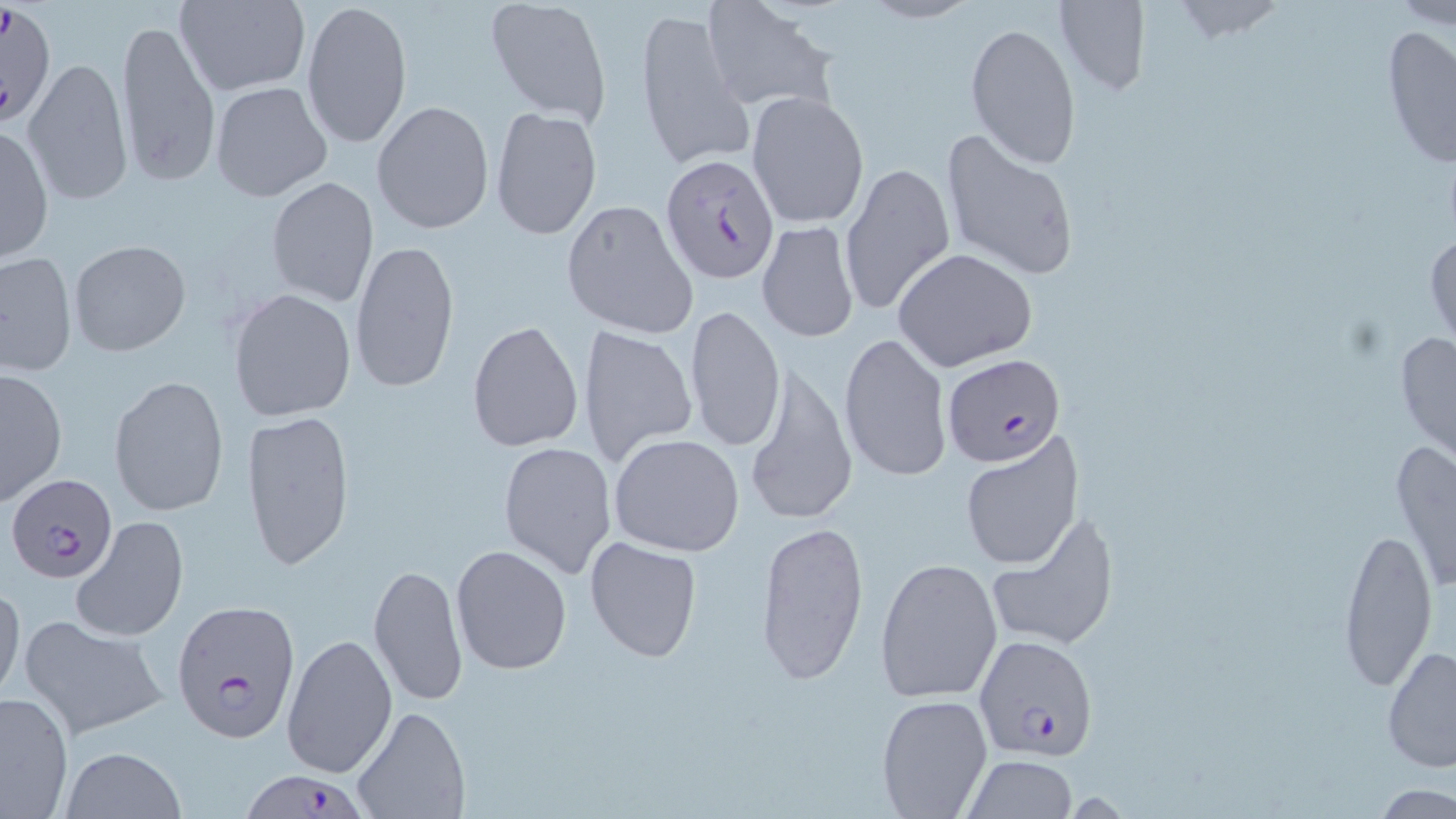
Summary:
  - Coordinate format: approximate bounding boxes as (x1, y1, x2, y2) in pixels
  - Uninfected red blood cell locations: (174, 0, 310, 96), (299, 0, 412, 149), (484, 0, 612, 124), (701, 0, 834, 112), (1054, 0, 1151, 97), (1167, 0, 1288, 41), (858, 1, 980, 25), (1389, 1, 1456, 28), (635, 5, 752, 171), (117, 17, 220, 188), (965, 22, 1081, 169), (1379, 24, 1456, 173), (23, 58, 135, 205), (209, 82, 333, 203), (746, 90, 870, 229), (371, 99, 494, 236), (490, 105, 603, 242), (0, 125, 53, 266), (938, 129, 1080, 281), (840, 163, 955, 317), (266, 177, 379, 308), (560, 198, 699, 340), (756, 221, 859, 344), (1425, 226, 1455, 356), (350, 238, 460, 395), (68, 240, 191, 356), (893, 248, 1038, 371), (1, 250, 77, 378), (228, 288, 357, 421), (685, 305, 785, 453), (467, 320, 584, 453), (577, 324, 698, 470), (1393, 325, 1456, 468), (839, 331, 952, 484), (741, 363, 857, 527), (1, 368, 68, 505), (109, 375, 230, 517), (243, 408, 354, 573), (959, 432, 1083, 571), (608, 433, 747, 557), (1388, 437, 1456, 596), (497, 442, 615, 578), (985, 508, 1119, 653), (71, 516, 189, 643), (755, 520, 870, 687), (1339, 521, 1439, 697), (585, 537, 703, 661), (450, 544, 572, 676), (875, 557, 1004, 704), (369, 562, 468, 705), (0, 582, 23, 706), (17, 615, 170, 740), (282, 633, 397, 776), (1381, 642, 1456, 774), (0, 691, 73, 817), (876, 694, 994, 818), (351, 703, 470, 819), (59, 747, 185, 819), (959, 755, 1079, 819), (1372, 782, 1456, 818)
  - Plasmodium falciparum-infected red blood cell locations: (2, 1, 57, 128), (658, 152, 778, 283), (942, 352, 1068, 467), (6, 474, 120, 588), (171, 601, 298, 742), (974, 635, 1100, 760), (231, 772, 366, 819)
  - Slide-level diagnosis: Plasmodium falciparum
  - Stain: May-Grünwald-Giemsa
  - Preparation: thin blood smear
  - Image size: 1456×819 pixels
  - Magnification: 1000x
  - Modality: optical microscopy
  - Field of view: single